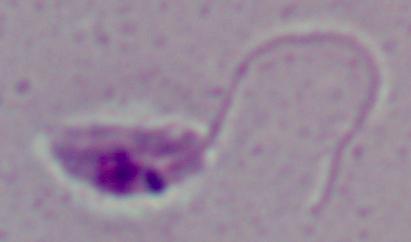 1000x magnification. A Leishmania parasite is shown. Micrograph.